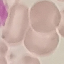

{
  "result": "negative for malaria parasites",
  "image_type": "cell patch, automatically extracted from a larger field of view and resized to 64 × 64 pixels",
  "stain": "Giemsa",
  "capture": "smartphone camera at the microscope eyepiece",
  "preparation": "thin smear"
}